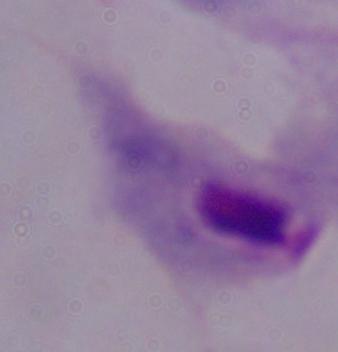
{
  "modality": "micrograph",
  "magnification": "1000x",
  "identification": "trichomonad"
}